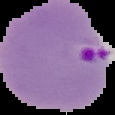
preparation: thin blood smear
image_type: segmented cell region with the area outside set to black
image_size: 115×115 pixels
result: malaria parasites identified